Locate every blood parasite and identify its species.
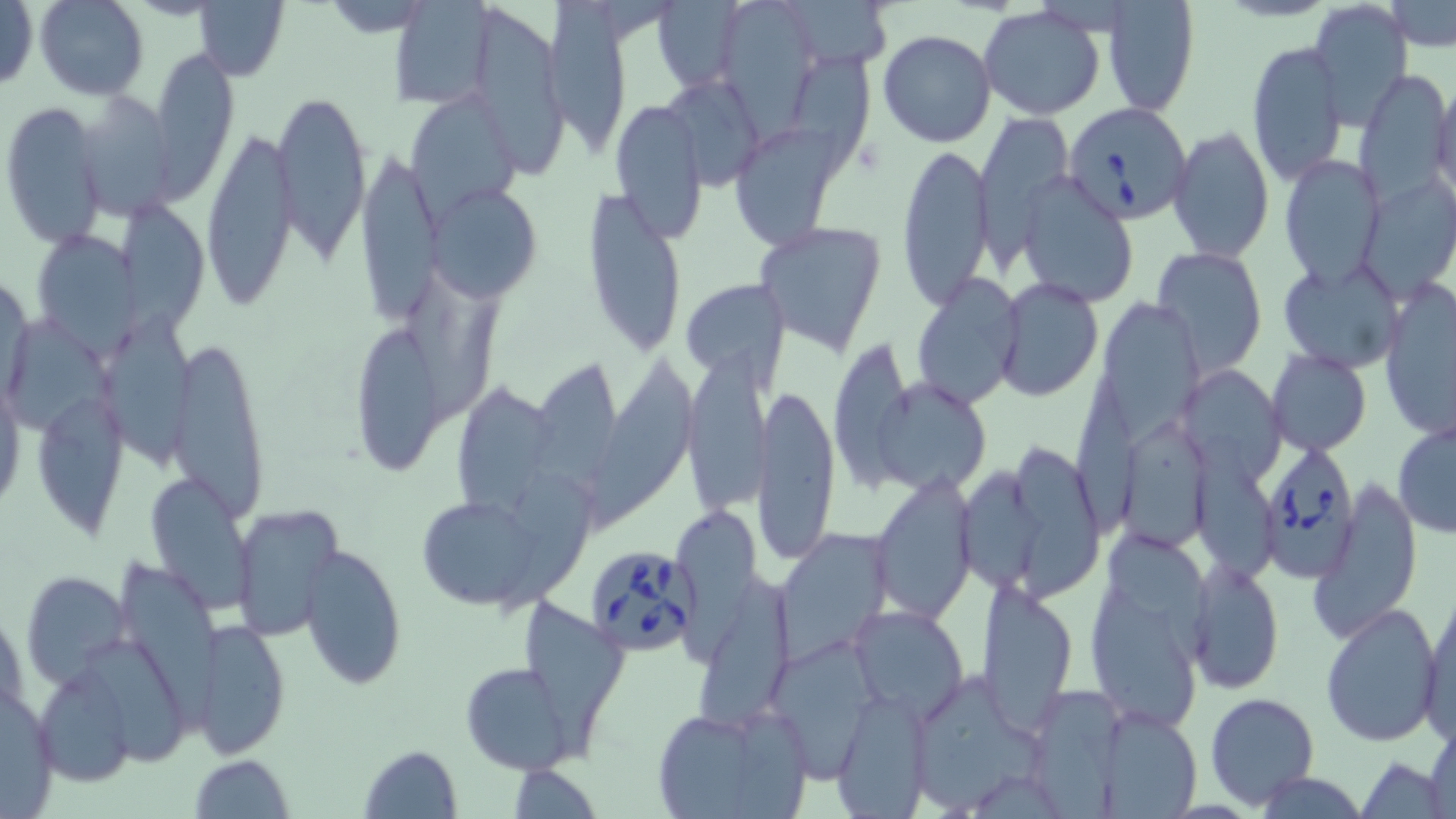
Approximate bounding boxes as (x1,y1)-(x2,y2) corner pairs in pixels.
Babesia divergens-infected red blood cells: (1063,101)-(1194,224), (1262,447)-(1365,585), (584,542)-(700,656).
No Plasmodium falciparum, Plasmodium ovale, Plasmodium malariae, Plasmodium vivax, or Trypanosoma brucei observed.

{
  "slide_level_diagnosis": "Babesia divergens",
  "image_size": "1456×819 pixels",
  "modality": "optical microscopy",
  "uninfected_red_blood_cell_locations": "approximate bounding boxes as (x1,y1)-(x2,y2) corner pairs in pixels: (652,0)-(744,90), (35,1)-(148,100), (387,1)-(498,111), (546,1)-(633,167), (1099,1)-(1199,114), (1310,1)-(1413,125), (0,2)-(39,92), (195,2)-(288,80), (1387,2)-(1455,50), (727,3)-(812,152), (978,7)-(1105,119), (465,8)-(570,180), (878,30)-(998,147), (1246,41)-(1347,185), (150,53)-(239,199), (791,53)-(878,192), (1355,68)-(1454,202), (1431,77)-(1456,201), (669,81)-(765,190), (271,87)-(373,263), (402,95)-(521,224), (81,96)-(186,221), (608,97)-(709,245), (2,101)-(106,249), (977,112)-(1074,245), (736,123)-(840,252), (1169,125)-(1274,263), (201,126)-(299,308), (896,142)-(994,311), (355,150)-(443,328), (1279,155)-(1387,288), (1018,172)-(1138,308), (1362,178)-(1455,299), (427,186)-(540,300), (582,191)-(687,358), (117,206)-(210,325), (754,221)-(891,360), (34,227)-(150,365), (1154,245)-(1267,372), (1278,258)-(1402,372), (678,277)-(791,384), (913,277)-(1026,413), (994,278)-(1103,402), (1378,279)-(1456,443), (404,285)-(503,425), (1098,297)-(1198,440), (349,315)-(444,476), (5,320)-(115,440), (104,324)-(195,470), (168,334)-(270,522), (834,344)-(915,493), (1267,350)-(1371,456), (682,352)-(773,513), (587,355)-(707,542), (533,356)-(622,497), (0,368)-(24,515), (1067,373)-(1156,527), (1189,375)-(1283,488), (863,377)-(995,494), (755,384)-(841,563), (456,389)-(556,523), (37,401)-(131,539), (1392,422)-(1456,538), (1122,426)-(1213,554), (1196,438)-(1281,592), (1012,447)-(1107,602), (958,465)-(1048,591), (493,466)-(597,629), (868,472)-(979,625), (146,474)-(256,611), (1311,480)-(1422,645), (408,491)-(565,612), (231,505)-(342,640), (671,508)-(765,675), (773,529)-(896,663), (1109,533)-(1218,665), (298,543)-(406,691), (120,556)-(222,738), (1187,559)-(1282,695), (21,572)-(133,690), (706,576)-(793,731), (977,578)-(1079,733), (1087,584)-(1202,731), (1419,592)-(1456,742), (523,599)-(628,761), (1318,601)-(1442,747), (847,604)-(971,721), (192,618)-(291,760), (773,640)-(885,780), (89,644)-(189,777), (461,661)-(575,774), (35,665)-(135,787), (919,675)-(1045,812), (0,682)-(61,819), (1041,686)-(1128,814), (1205,692)-(1319,809), (830,693)-(932,818), (1096,707)-(1204,819), (652,708)-(794,818), (1425,720)-(1456,819), (357,744)-(463,818), (1358,754)-(1449,818), (188,756)-(294,818), (508,763)-(601,816), (1254,768)-(1369,819)",
  "stain": "May-Grünwald-Giemsa",
  "preparation": "thin blood smear",
  "field_of_view": "single",
  "magnification": "1000x"
}